Identify the parasite.
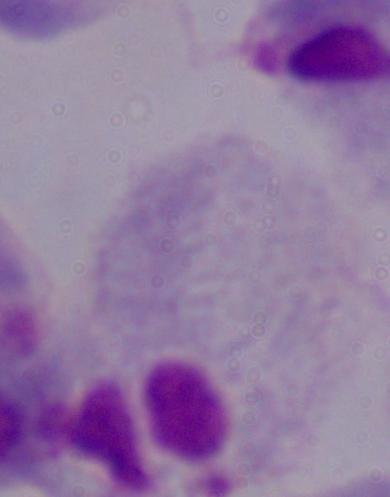

A trichomonad.

Micrograph. Captured at 1000x magnification.